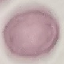

Summary:
  - Malaria status: uninfected
  - Image type: cell patch, automatically extracted from a larger field of view and resized to 64 × 64 pixels
  - Capture: smartphone camera at the microscope eyepiece
  - Stain: Giemsa
  - Preparation: thin smear